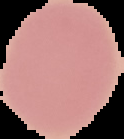

From a thin blood film. Malaria status: uninfected. The area outside the segmented cell region is set to black. Image is 124×139 pixels.